State which parasite is depicted.
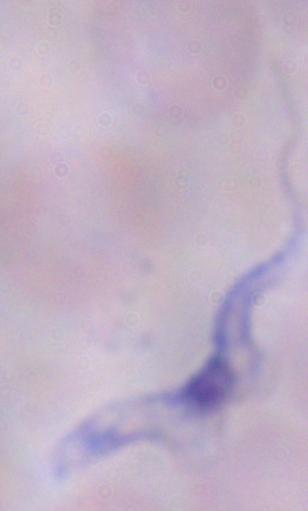

A trypanosome.

1000x magnification. Micrograph.